Report the malaria status of this cell.
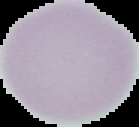
Uninfected.

Summary:
  - Image size: 139×127 pixels
  - Image type: segmented cell region with the area outside set to black
  - Preparation: thin blood film